State which parasite is depicted.
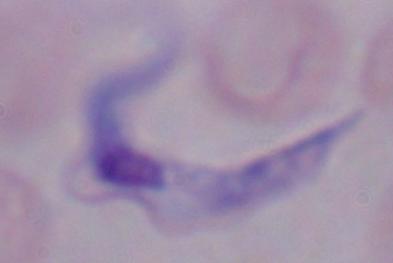
A trypanosome.

1000x magnification. Photomicrograph.